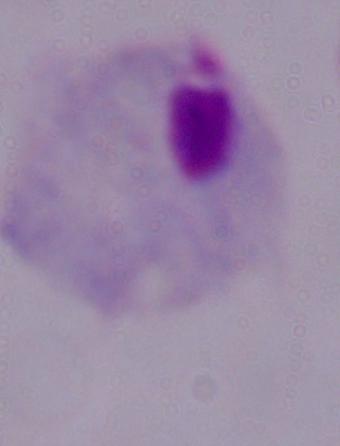

Captured at 1000x magnification. A trichomonad is shown. Micrograph.